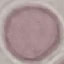 Result: no malaria parasites seen. Giemsa stain. Thin blood smear. Acquired by smartphone through the microscope eyepiece. Automatically extracted cell patch, resized to 64 × 64 pixels.